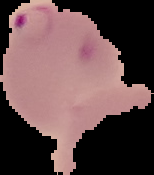

image_size: 154×175 pixels
image_type: cell region segmented out of the field of view; surrounding area masked to black
preparation: thin blood smear
result: Plasmodium parasites identified